Assess the morphology of the erythrocytes.
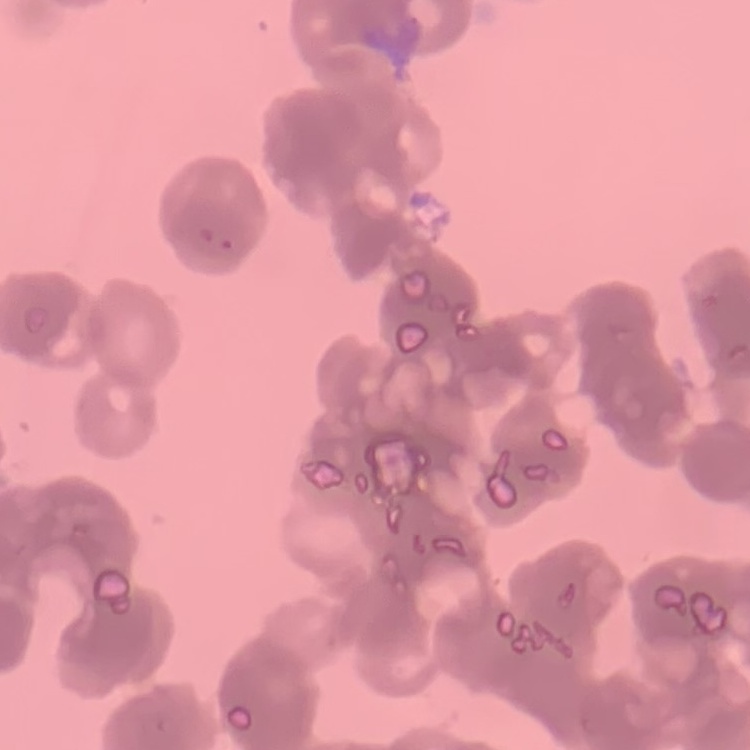
Rouleaux formation.

Summary:
  - Image type: one tile cut from a larger photomicrograph
  - Preparation: thin peripheral smear
  - Stain: Field's or Giemsa